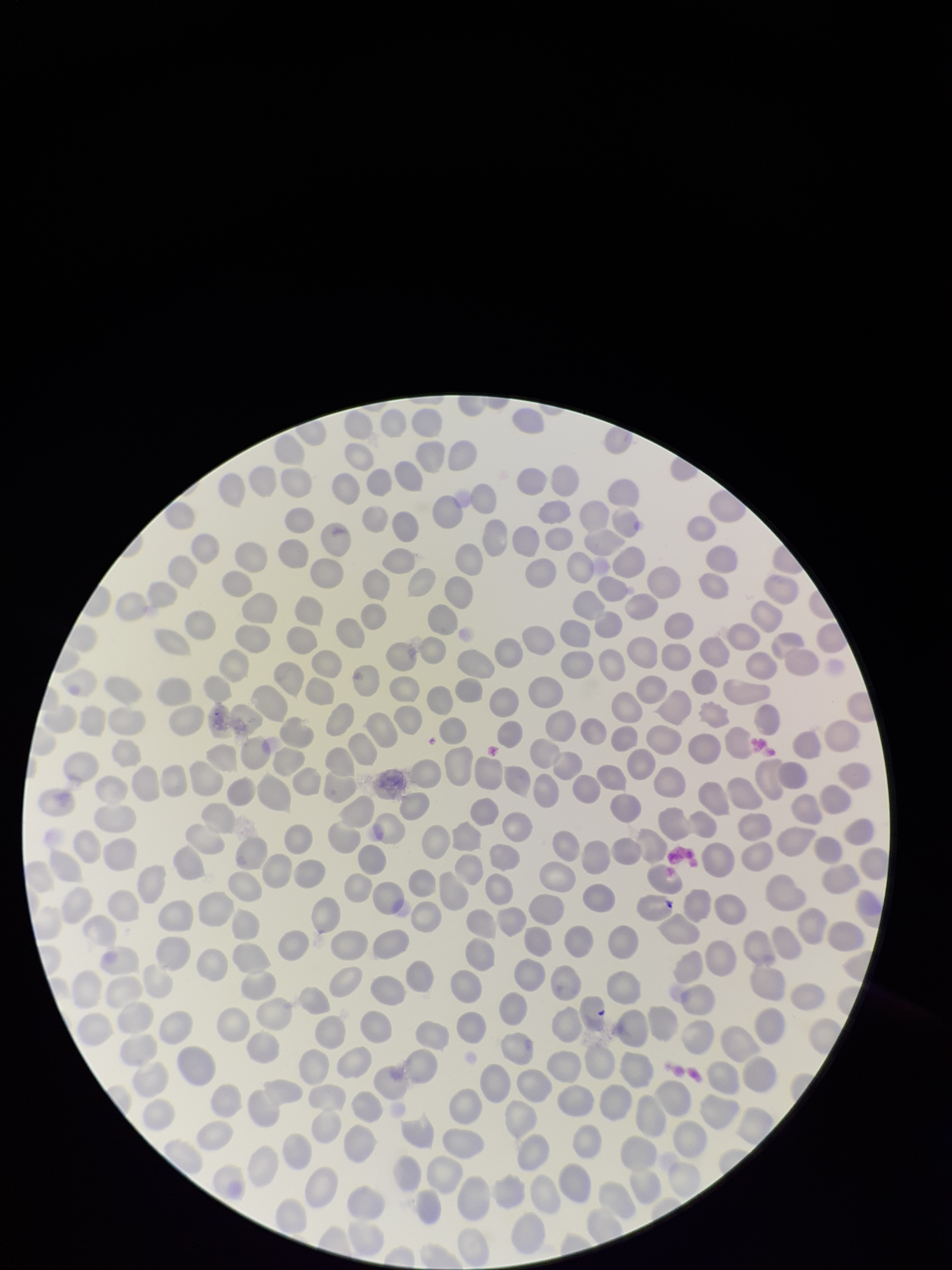
red blood cell count = 289
preparation = thin smear
patient malaria status = negative
field of view = single
capture = smartphone photograph through the microscope eyepiece
image size = 952×1270 pixels
stain = Giemsa
parasitized red blood cells = none detected
parasitized red blood cell count = 0